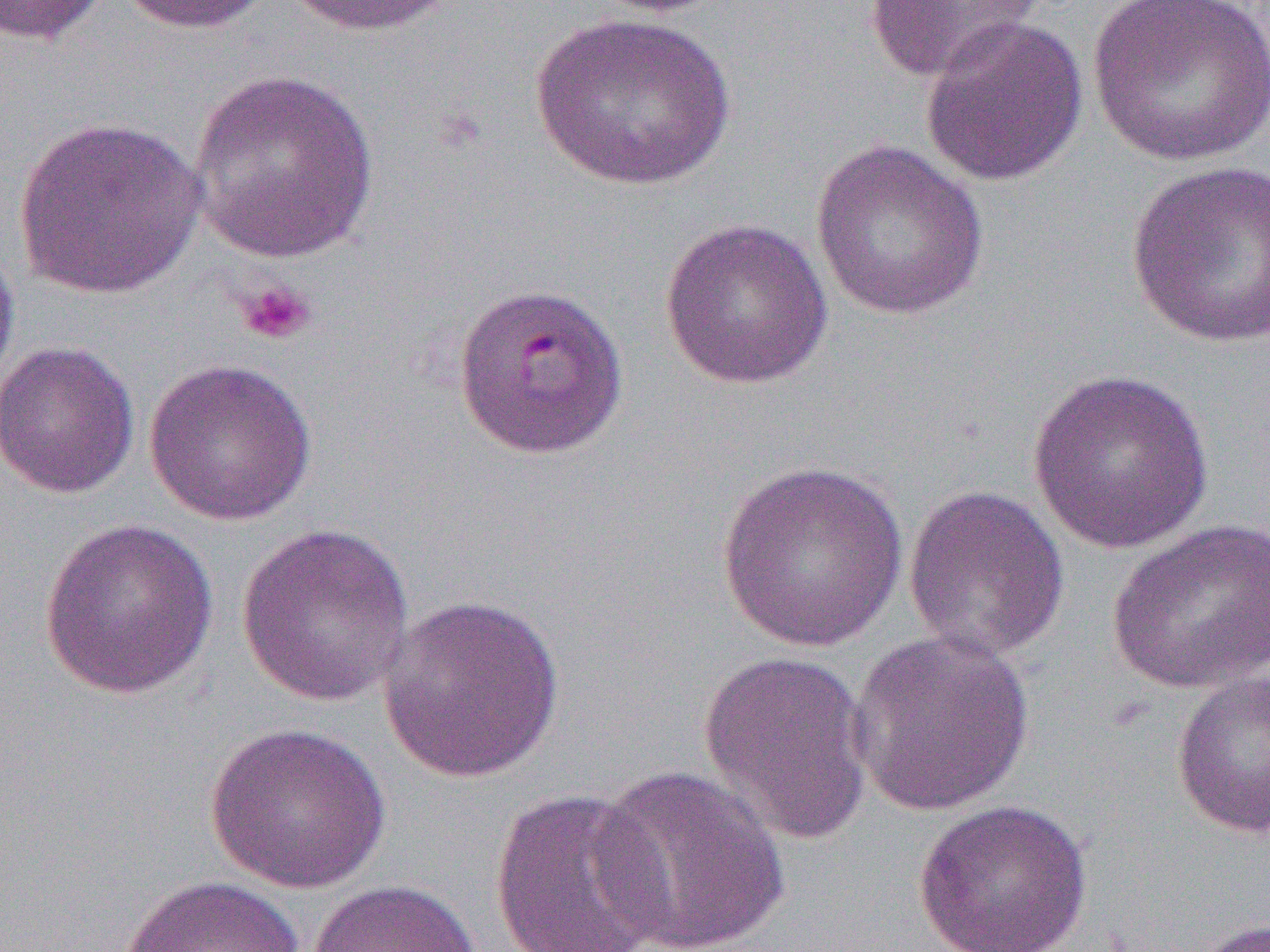 Approximate bounding boxes as (x1, y1, x2, y2) in pixels. Platelet locations: (234, 279, 316, 345). Uninfected red blood cell locations (subset): (0, 0, 113, 46), (112, 0, 272, 35), (284, 0, 459, 38), (581, 0, 737, 18), (865, 0, 1045, 83), (1088, 0, 1270, 168), (529, 11, 738, 192), (919, 16, 1090, 188), (187, 68, 381, 263), (14, 116, 206, 300), (810, 138, 989, 321), (1125, 159, 1270, 351), (658, 217, 834, 390), (0, 237, 21, 395), (0, 340, 141, 500), (142, 357, 318, 526), (1026, 368, 1214, 554), (715, 459, 908, 652), (902, 484, 1070, 663), (39, 518, 219, 700), (1105, 518, 1270, 695), (236, 522, 415, 707), (377, 593, 565, 782), (848, 629, 1036, 817), (697, 649, 875, 845), (1170, 669, 1270, 841), (204, 721, 393, 893), (590, 765, 790, 952), (488, 786, 672, 952), (912, 799, 1094, 952), (116, 875, 308, 952), (305, 880, 481, 952), (1193, 915, 1270, 952). Slide-level diagnosis: Plasmodium falciparum. Optical microscopy. Captured at 1000x magnification. Thin blood film. Single field of view. Image is 1270×952 pixels.